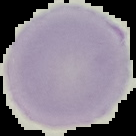 The area outside the segmented cell region is set to black. Image is 136×136 pixels. From a thin blood smear. Result: no malaria parasites detected.